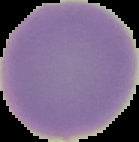
Result: negative for Plasmodium parasites. The area outside the segmented cell region is set to black. Image is 139×142 pixels. From a thin blood smear.